Locate every blood parasite and identify its species.
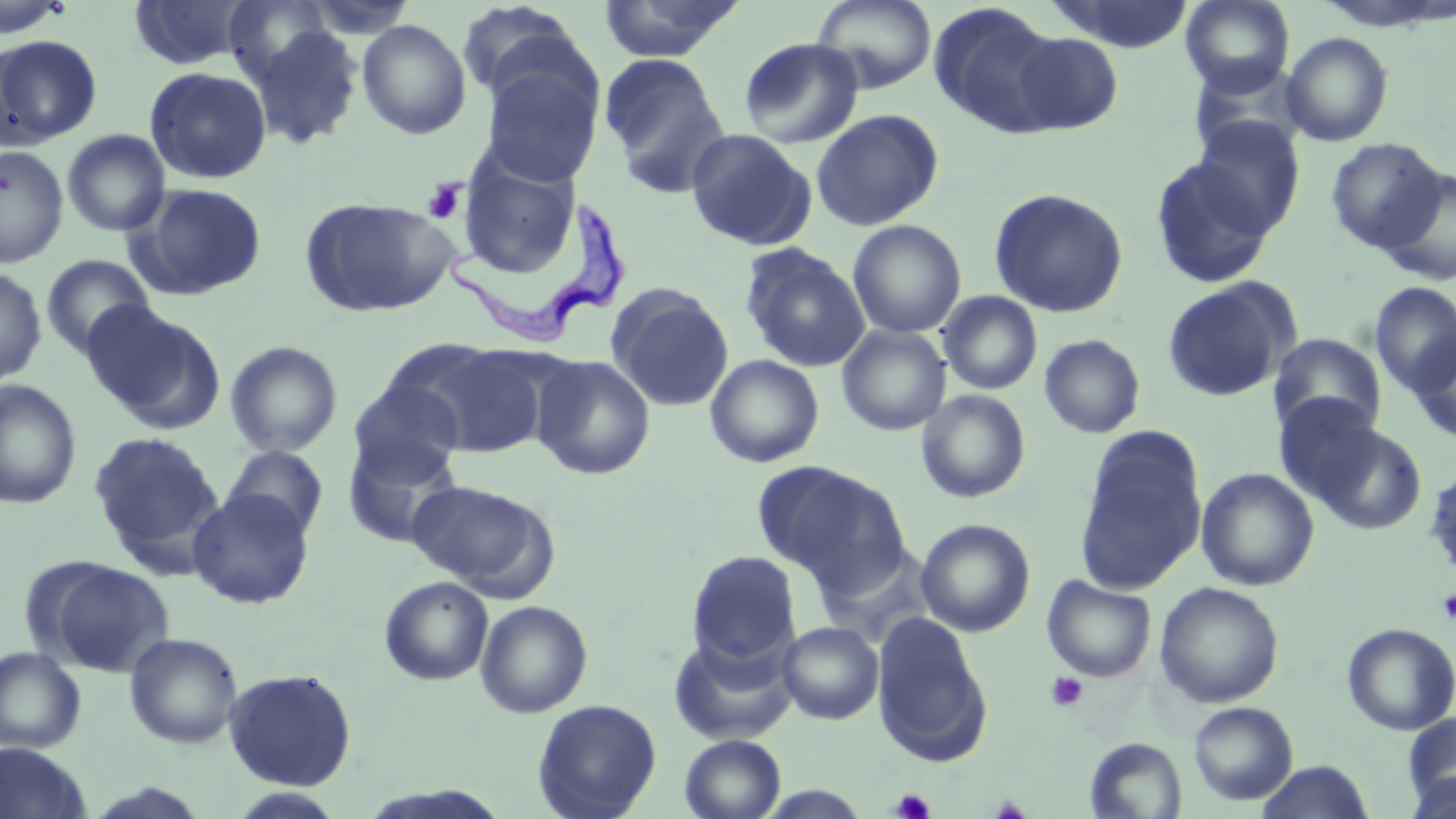
Approximate bounding boxes as [x1, y1, x2, y2] in pixels.
Trypanosoma brucei: [441, 199, 633, 347].
No Plasmodium falciparum, Plasmodium ovale, Plasmodium malariae, Plasmodium vivax, or Babesia divergens observed.

{
  "slide_level_diagnosis": "Trypanosoma brucei",
  "magnification": "1000x",
  "image_size": "1456×819 pixels",
  "stain": "May-Grünwald-Giemsa",
  "platelet_locations": "approximate bounding boxes as [x1, y1, x2, y2] in pixels: [421, 178, 467, 224], [1437, 589, 1456, 624], [1046, 672, 1089, 713], [890, 788, 935, 818]",
  "field_of_view": "single",
  "modality": "optical microscopy",
  "uninfected_red_blood_cell_locations": "approximate bounding boxes as [x1, y1, x2, y2] in pixels: [0, 0, 73, 39], [221, 0, 336, 87], [596, 0, 745, 63], [811, 0, 937, 94], [1054, 0, 1196, 53], [1180, 0, 1295, 97], [128, 1, 253, 70], [928, 3, 1065, 138], [457, 6, 596, 124], [356, 19, 472, 139], [250, 25, 364, 150], [1282, 31, 1394, 147], [1010, 32, 1123, 135], [0, 35, 102, 148], [739, 37, 864, 149], [599, 53, 731, 197], [478, 54, 603, 187], [144, 67, 272, 184], [810, 109, 944, 230], [835, 110, 957, 336], [1190, 116, 1305, 236], [685, 128, 816, 250], [62, 130, 171, 236], [1325, 137, 1447, 253], [0, 144, 68, 267], [1149, 156, 1275, 289], [457, 158, 583, 278], [1378, 168, 1456, 285], [132, 183, 267, 299], [989, 188, 1129, 318], [300, 196, 458, 318], [847, 220, 966, 338], [741, 244, 870, 372], [41, 254, 155, 360], [0, 266, 47, 387], [1162, 278, 1297, 402], [1370, 281, 1456, 395], [607, 285, 734, 411], [938, 291, 1042, 395], [83, 302, 223, 433], [836, 325, 951, 436], [1409, 331, 1456, 444], [1269, 333, 1386, 436], [1039, 334, 1145, 438], [225, 341, 343, 456], [416, 344, 549, 459], [532, 355, 656, 480], [705, 355, 824, 467], [0, 379, 81, 509], [349, 380, 464, 486], [916, 390, 1031, 503], [1272, 393, 1385, 503], [1311, 422, 1428, 536], [89, 432, 221, 559], [342, 435, 462, 548], [1074, 435, 1207, 594], [222, 444, 329, 541], [754, 459, 910, 593], [1422, 464, 1456, 581], [1196, 467, 1320, 591], [407, 480, 557, 597], [188, 488, 315, 609], [916, 518, 1036, 637], [686, 550, 801, 669], [41, 559, 174, 677], [1042, 575, 1156, 682], [379, 576, 494, 686], [1154, 581, 1284, 708], [475, 599, 593, 718], [872, 613, 992, 764], [778, 621, 884, 724], [1341, 622, 1456, 735], [123, 632, 244, 749], [669, 635, 798, 745], [0, 646, 86, 752], [223, 667, 358, 790], [531, 699, 662, 819], [1188, 701, 1298, 805], [1402, 712, 1456, 810], [680, 734, 786, 819], [1085, 737, 1187, 818], [0, 742, 92, 819], [1255, 760, 1375, 819], [1404, 773, 1456, 819], [225, 788, 350, 818]",
  "preparation": "thin blood smear"
}